Assess the morphology of the erythrocytes.
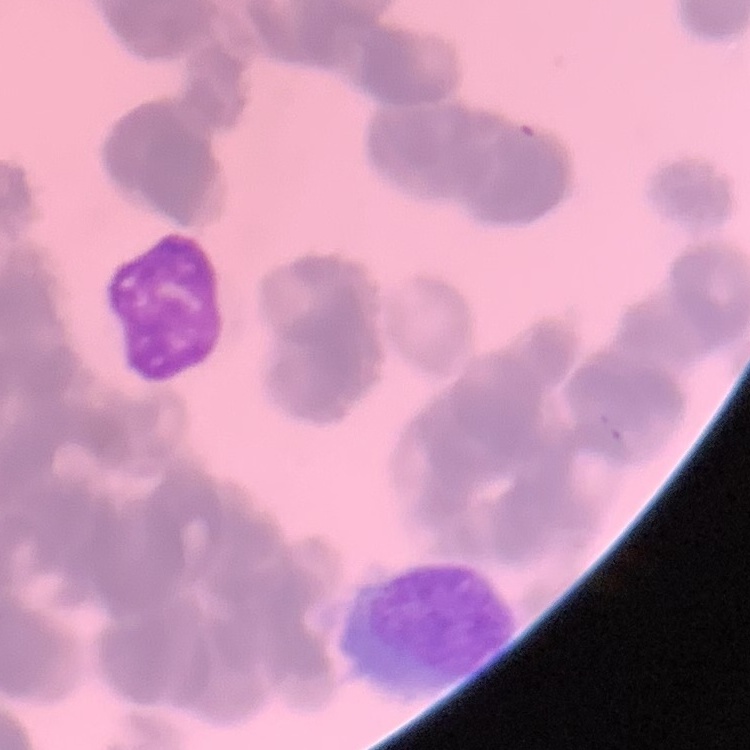

Rouleaux formation.

image type = one tile cut from a larger photomicrograph
preparation = thin peripheral smear
stain = Field's or Giemsa